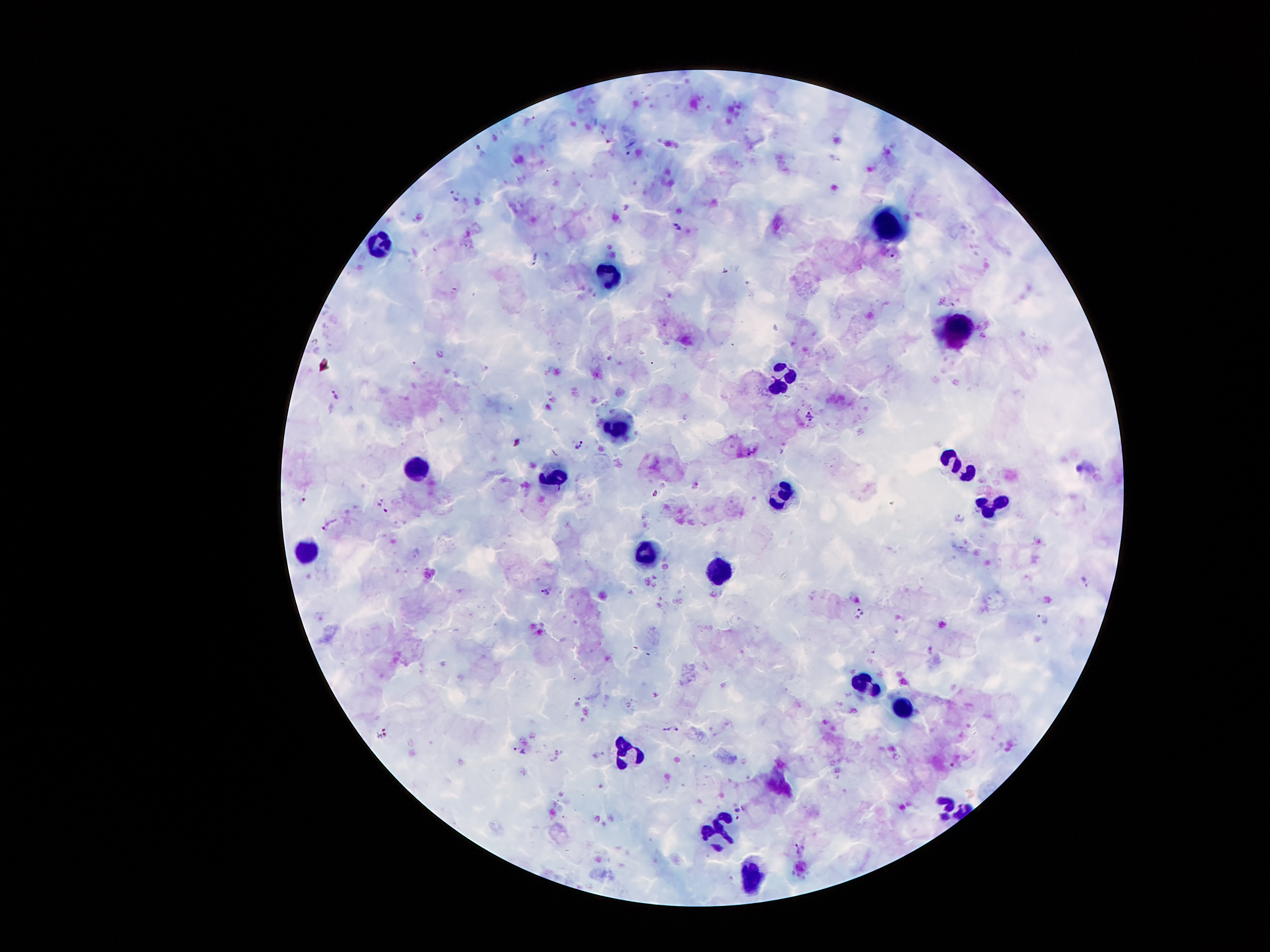

Approximate object centers, in pixels from the top-left corner. Leukocyte locations: (x=887, y=223), (x=383, y=243), (x=612, y=275), (x=957, y=330), (x=785, y=376), (x=618, y=425), (x=954, y=458), (x=417, y=468), (x=556, y=475), (x=968, y=475), (x=782, y=491), (x=993, y=506), (x=647, y=552), (x=309, y=556), (x=720, y=569), (x=867, y=682), (x=902, y=707), (x=628, y=750), (x=944, y=805), (x=717, y=830), (x=751, y=877). Malaria parasite locations: (x=454, y=195), (x=680, y=227), (x=537, y=260), (x=336, y=395), (x=810, y=416), (x=580, y=445), (x=546, y=591), (x=738, y=814). One field from this slide. Giemsa-stained preparation. Photographed through the microscope eyepiece with a smartphone camera. Patient malaria status: positive for Plasmodium falciparum. 100x magnification. Image is 1270×952 pixels. Thick blood smear.